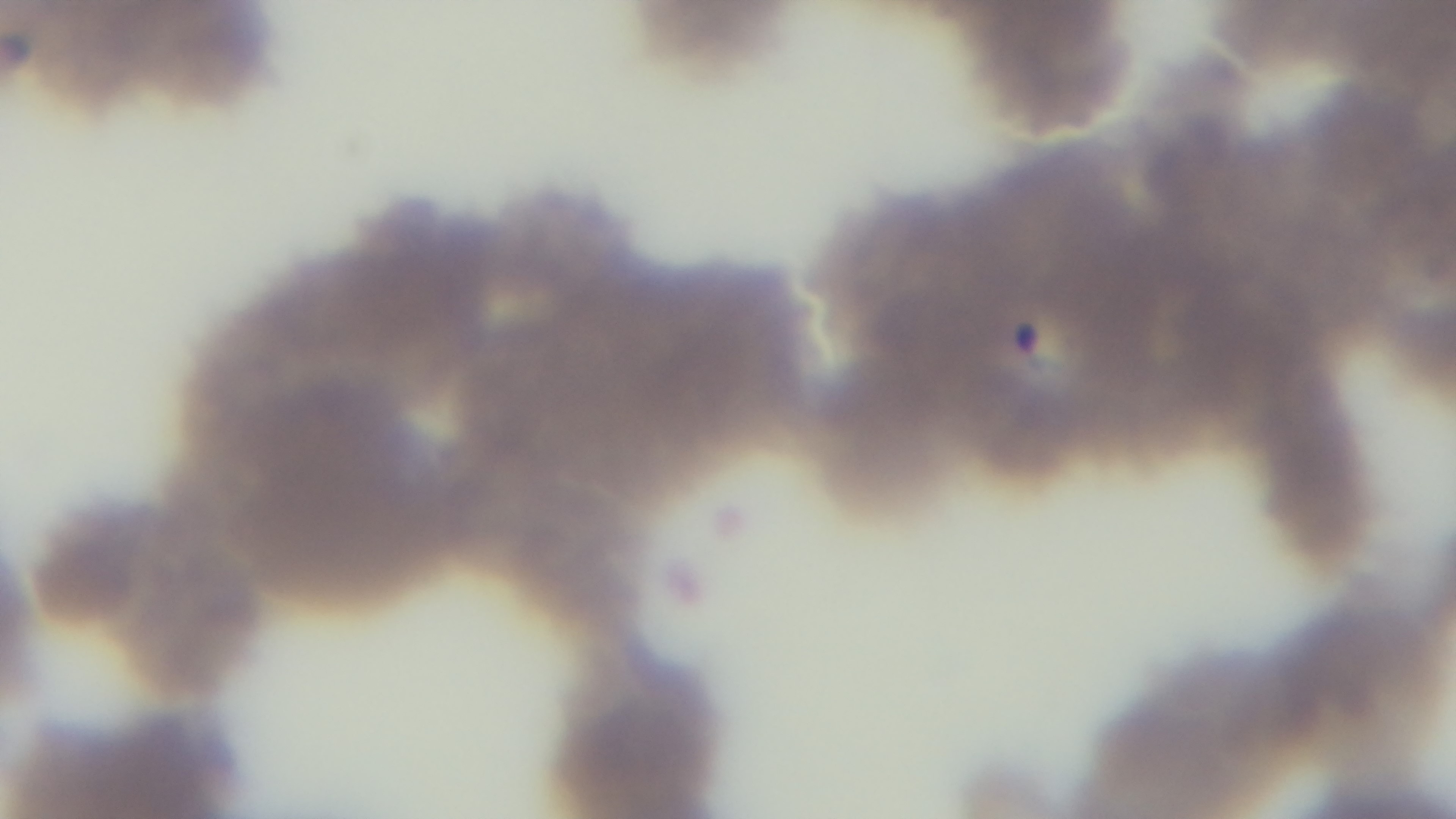
Summary:
  - Objective: 100x oil immersion
  - Field of view: single
  - Stain: Giemsa
  - Capture: mounted 4K digital camera
  - Malaria status: positive
  - Modality: light microscopy
  - Preparation: thin smear